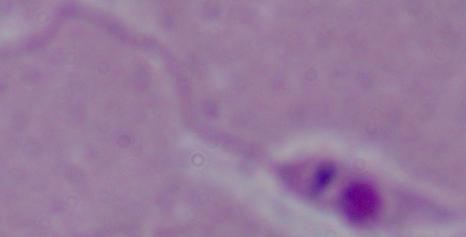
Summary:
  - Magnification: 1000x
  - Modality: micrograph
  - Identification: Leishmania